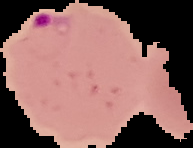 From a thin blood film. Image is 193×148 pixels. Result: malaria parasites detected. The area outside the segmented cell region is set to black.